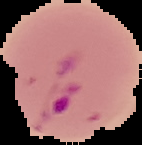

Summary:
  - Result: malaria parasites detected
  - Image type: segmented cell region with the area outside set to black
  - Image size: 142×145 pixels
  - Preparation: thin blood film